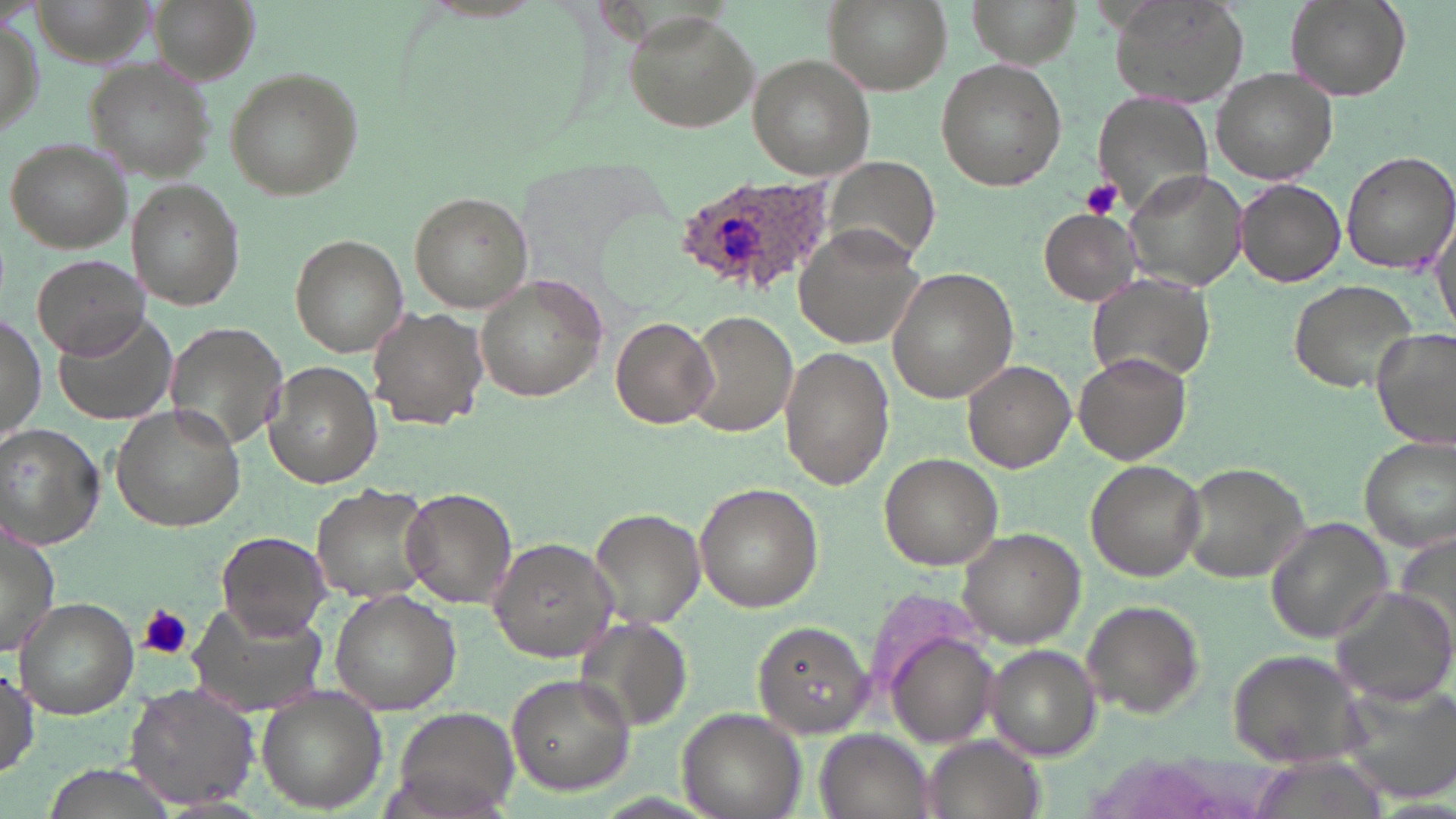 Approximate bounding boxes as (x1,y1)-(x2,y2) corner pairs in pixels. Plasmodium ovale-infected red blood cell locations: (675,173)-(838,295). Platelet locations: (1082,179)-(1123,219), (138,604)-(193,661). Uninfected red blood cell locations: (29,0)-(157,73), (150,0)-(256,84), (822,0)-(951,96), (969,0)-(1080,67), (1107,0)-(1251,109), (1285,0)-(1410,100), (624,13)-(759,133), (747,56)-(874,178), (84,57)-(215,180), (935,58)-(1067,193), (224,65)-(365,202), (1211,69)-(1338,183), (1095,91)-(1217,215), (5,137)-(131,252), (1341,151)-(1456,274), (825,156)-(942,265), (1124,169)-(1248,293), (1235,178)-(1346,287), (129,179)-(244,309), (410,190)-(532,314), (1039,209)-(1140,305), (798,226)-(929,348), (290,234)-(410,356), (32,253)-(148,361), (886,267)-(1019,402), (475,273)-(607,403), (1088,275)-(1213,380), (1287,278)-(1424,394), (368,306)-(487,428), (54,309)-(180,424), (687,310)-(800,439), (0,312)-(46,449), (611,314)-(717,429), (165,322)-(289,454), (1370,324)-(1454,452), (779,345)-(892,490), (1074,352)-(1191,465), (263,359)-(380,488), (961,359)-(1077,473), (109,403)-(245,532), (0,423)-(105,549), (1357,438)-(1455,552), (880,452)-(1002,570), (1085,460)-(1206,581), (1180,461)-(1314,585), (313,482)-(437,606), (695,482)-(821,611), (399,486)-(518,610), (589,508)-(707,631), (1264,517)-(1395,645), (0,519)-(60,654), (957,526)-(1085,648), (1392,527)-(1455,658), (217,529)-(331,641), (488,535)-(623,663), (1329,589)-(1456,708), (330,591)-(460,714), (14,597)-(137,718), (1080,599)-(1205,720), (192,604)-(331,714), (578,616)-(692,732), (754,620)-(876,736), (884,633)-(1004,747), (986,644)-(1101,762), (1225,648)-(1375,772), (1,667)-(40,779), (506,672)-(635,795), (124,681)-(261,810), (1342,685)-(1456,806), (255,690)-(388,812), (678,706)-(806,819), (391,711)-(518,817), (816,730)-(933,819), (920,735)-(1046,819), (40,763)-(170,817). Slide-level diagnosis: Plasmodium ovale. Image is 1456×819 pixels. Thin blood film. May-Grünwald-Giemsa-stained preparation. One field of a larger specimen. Light microscopy. 1000x magnification.